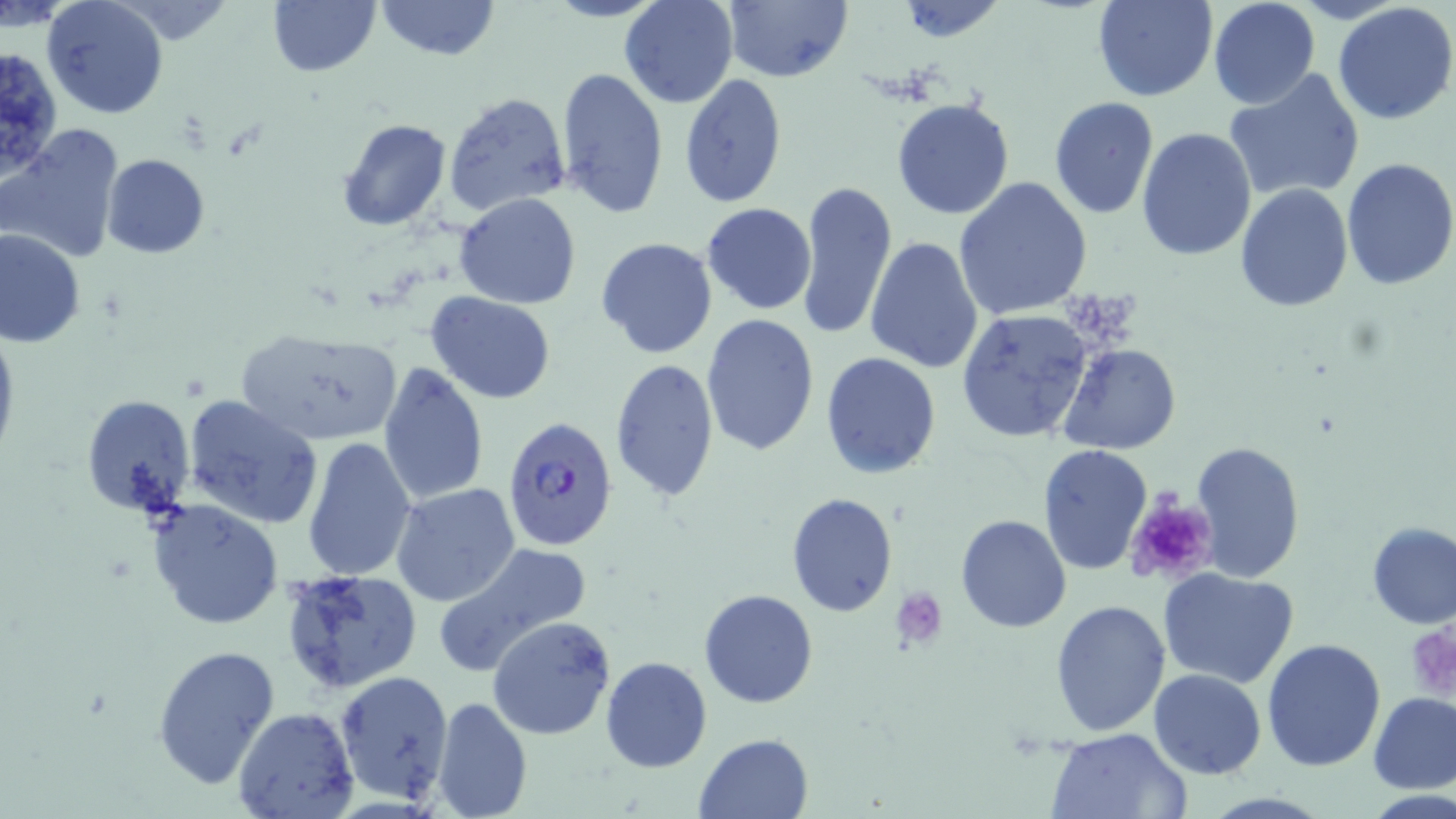
slide-level diagnosis = Plasmodium falciparum
preparation = thin blood film
platelet locations = approximate bounding boxes as (x1, y1, x2, y2) in pixels: (1124, 497, 1218, 586), (890, 585, 947, 647), (1411, 622, 1456, 701)
magnification = 1000x
image size = 1456×819 pixels
Plasmodium falciparum-infected red blood cell locations = approximate bounding boxes as (x1, y1, x2, y2) in pixels: (501, 415, 619, 549)
uninfected red blood cell locations = approximate bounding boxes as (x1, y1, x2, y2) in pixels: (43, 0, 170, 119), (266, 0, 380, 78), (377, 0, 497, 61), (543, 0, 666, 23), (618, 0, 740, 109), (722, 0, 851, 82), (1091, 0, 1217, 102), (1207, 0, 1320, 109), (896, 1, 1008, 45), (1332, 2, 1456, 124), (0, 44, 64, 178), (554, 66, 669, 219), (1225, 68, 1365, 203), (679, 72, 788, 207), (443, 90, 572, 215), (1048, 97, 1160, 221), (892, 99, 1016, 220), (337, 119, 451, 233), (1, 125, 127, 264), (1136, 128, 1257, 262), (102, 155, 210, 259), (1340, 159, 1456, 290), (953, 176, 1093, 322), (796, 178, 898, 342), (1234, 184, 1354, 311), (454, 193, 582, 309), (701, 202, 816, 314), (0, 228, 87, 348), (595, 236, 718, 359), (866, 236, 984, 372), (427, 291, 556, 403), (700, 311, 819, 457), (956, 311, 1093, 441), (0, 321, 20, 468), (233, 326, 403, 446), (1058, 342, 1181, 454), (821, 351, 941, 478), (609, 359, 720, 505), (376, 363, 488, 506), (81, 393, 197, 519), (183, 395, 325, 529), (301, 435, 417, 583), (1191, 439, 1305, 581), (1038, 444, 1152, 577), (392, 483, 521, 607), (787, 492, 898, 616), (147, 499, 282, 631), (955, 514, 1071, 633), (1365, 521, 1456, 630), (432, 540, 592, 675), (1157, 566, 1299, 688), (280, 568, 424, 694), (698, 589, 819, 708), (1050, 599, 1171, 736), (488, 615, 617, 740), (1261, 639, 1388, 772), (150, 643, 281, 791), (601, 657, 712, 773), (1149, 668, 1266, 779), (335, 670, 453, 805), (1368, 691, 1456, 795), (431, 696, 530, 819), (233, 706, 358, 819), (1046, 728, 1189, 817), (694, 733, 813, 819)
field of view = single
stain = May-Grünwald-Giemsa
modality = light microscopy